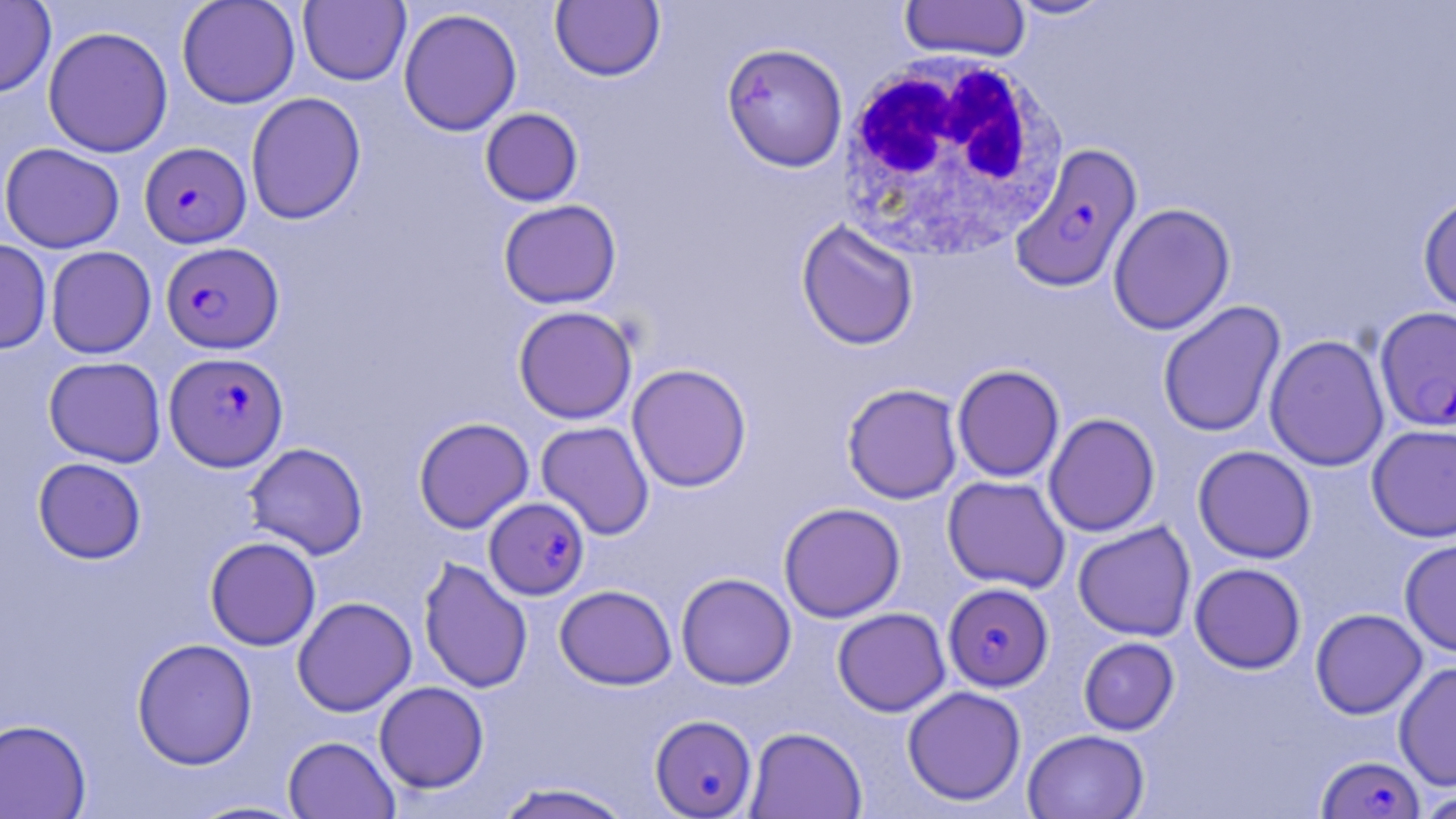

Approximate bounding boxes as (x1, y1, x2, y2) in pixels. Plasmodium falciparum-infected red blood cell locations: (1010, 141, 1144, 292), (139, 142, 251, 248), (161, 242, 283, 353), (1374, 306, 1456, 433), (164, 351, 289, 472), (484, 495, 590, 600), (943, 583, 1053, 692), (649, 714, 758, 818), (1317, 755, 1425, 818). White blood cell locations: (833, 52, 1069, 263). Uninfected red blood cell locations: (0, 0, 56, 98), (176, 0, 301, 109), (1004, 0, 1117, 20), (298, 1, 411, 86), (550, 1, 665, 82), (899, 1, 1031, 62), (398, 7, 523, 136), (42, 25, 174, 158), (721, 42, 848, 172), (245, 92, 366, 225), (480, 108, 583, 207), (0, 142, 125, 253), (1417, 192, 1456, 315), (498, 199, 621, 309), (1108, 202, 1235, 335), (796, 219, 919, 351), (0, 239, 52, 354), (45, 245, 156, 359), (1157, 300, 1286, 438), (513, 306, 638, 424), (1264, 334, 1389, 472), (43, 356, 167, 467), (627, 363, 752, 492), (952, 364, 1065, 482), (842, 383, 963, 504), (1043, 412, 1160, 537), (413, 417, 534, 533), (536, 421, 655, 540), (1366, 423, 1456, 542), (244, 442, 369, 560), (1193, 445, 1316, 563), (32, 457, 147, 564), (942, 475, 1070, 593), (778, 502, 906, 622), (1072, 521, 1196, 642), (205, 536, 321, 650), (1399, 538, 1456, 657), (418, 557, 533, 694), (1189, 562, 1306, 674), (676, 572, 796, 689), (554, 585, 677, 689), (292, 596, 417, 717), (832, 607, 950, 716), (1310, 608, 1427, 719), (131, 637, 258, 770), (1078, 637, 1179, 736), (1394, 661, 1456, 791), (374, 681, 489, 793), (902, 686, 1027, 806), (0, 718, 92, 818), (745, 726, 867, 819), (1022, 729, 1149, 819), (282, 735, 399, 818), (491, 781, 637, 819), (1414, 789, 1456, 819), (185, 799, 311, 818). Slide-level diagnosis: Plasmodium falciparum. Light microscopy. Image is 1456×819 pixels. Single field of view. May-Grünwald-Giemsa-stained preparation. 1000x magnification. Thin blood film.